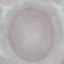
Summary:
  - Malaria status: uninfected
  - Stain: Giemsa
  - Capture: smartphone camera at the microscope eyepiece
  - Image type: automatically extracted cell patch, resized to 64 × 64 pixels
  - Preparation: thin smear